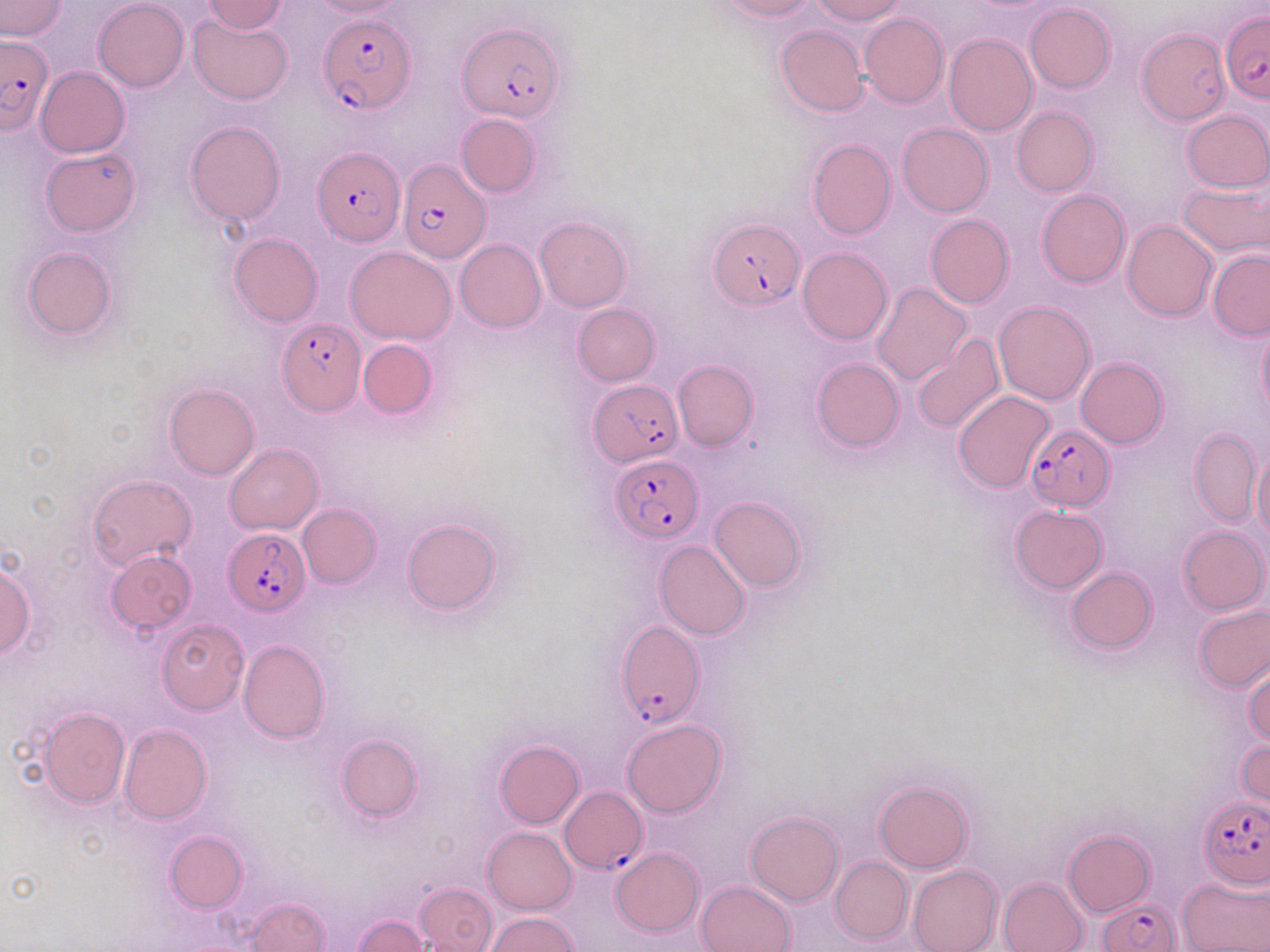
Summary:
  - Coordinate format: approximate bounding boxes as (x1,y1)-(x2,y2) corner pairs in pixels
  - Uninfected red blood cell locations: (93,0)-(189,90), (201,0)-(289,34), (719,0)-(819,21), (812,0)-(906,24), (0,1)-(66,41), (307,1)-(409,19), (1024,3)-(1115,93), (189,13)-(294,105), (859,13)-(949,107), (775,25)-(869,117), (1137,28)-(1229,129), (944,33)-(1036,136), (36,67)-(129,157), (1012,107)-(1097,196), (1181,110)-(1269,192), (456,114)-(539,197), (185,120)-(286,225), (897,122)-(994,218), (807,138)-(895,240), (42,148)-(141,237), (1179,180)-(1269,259), (1037,189)-(1129,287), (1082,204)-(1193,308), (925,214)-(1015,308), (535,216)-(631,312), (1122,221)-(1218,322), (451,229)-(628,321), (229,232)-(323,327), (454,238)-(546,332), (22,245)-(117,340), (346,247)-(456,345), (797,247)-(892,345), (1208,249)-(1270,339), (872,282)-(971,386), (993,300)-(1096,406), (572,303)-(659,385), (1257,321)-(1270,419), (912,333)-(1005,437), (358,338)-(438,417), (1076,356)-(1168,449), (812,358)-(904,451), (674,360)-(758,450), (164,383)-(259,481), (953,391)-(1055,492), (1189,427)-(1261,526), (225,443)-(322,534), (1252,448)-(1270,544), (88,474)-(196,571), (709,496)-(807,591), (297,503)-(380,587), (1010,505)-(1108,594), (403,519)-(501,614), (1178,526)-(1268,615), (654,540)-(749,640), (106,550)-(197,633), (1,562)-(35,659), (1067,567)-(1157,655), (1193,604)-(1270,691), (156,618)-(249,713), (239,641)-(330,743), (1244,662)-(1270,747), (38,709)-(130,807), (622,718)-(727,817), (119,724)-(211,823), (335,734)-(422,822), (1237,739)-(1270,811), (494,740)-(585,828), (875,780)-(972,872), (746,810)-(844,906), (483,826)-(576,915), (1064,829)-(1154,916), (165,831)-(247,911), (611,847)-(703,937), (830,856)-(911,944), (907,864)-(1002,952), (997,877)-(1089,952), (1178,877)-(1270,952), (696,880)-(797,952), (415,882)-(497,952), (246,896)-(328,952), (485,912)-(581,952), (354,914)-(430,952)
  - Plasmodium falciparum-infected red blood cell locations: (317,12)-(415,115), (1220,13)-(1270,102), (458,21)-(565,122), (1,35)-(53,134), (313,148)-(404,246), (397,158)-(491,267), (709,220)-(804,310), (278,318)-(365,415), (589,380)-(681,466), (1025,423)-(1114,511), (609,451)-(702,542), (222,528)-(310,614), (615,623)-(704,727), (558,786)-(646,874), (1199,798)-(1268,885), (1098,898)-(1179,952)
  - Slide-level diagnosis: Plasmodium falciparum
  - Preparation: thin blood smear
  - Image size: 1270×952 pixels
  - Field of view: single
  - Stain: May-Grünwald-Giemsa
  - Magnification: 1000x
  - Modality: light microscopy